Give the position of every malaria parasite, noting whether each is a trophozoite, schizont, or gametocyte.
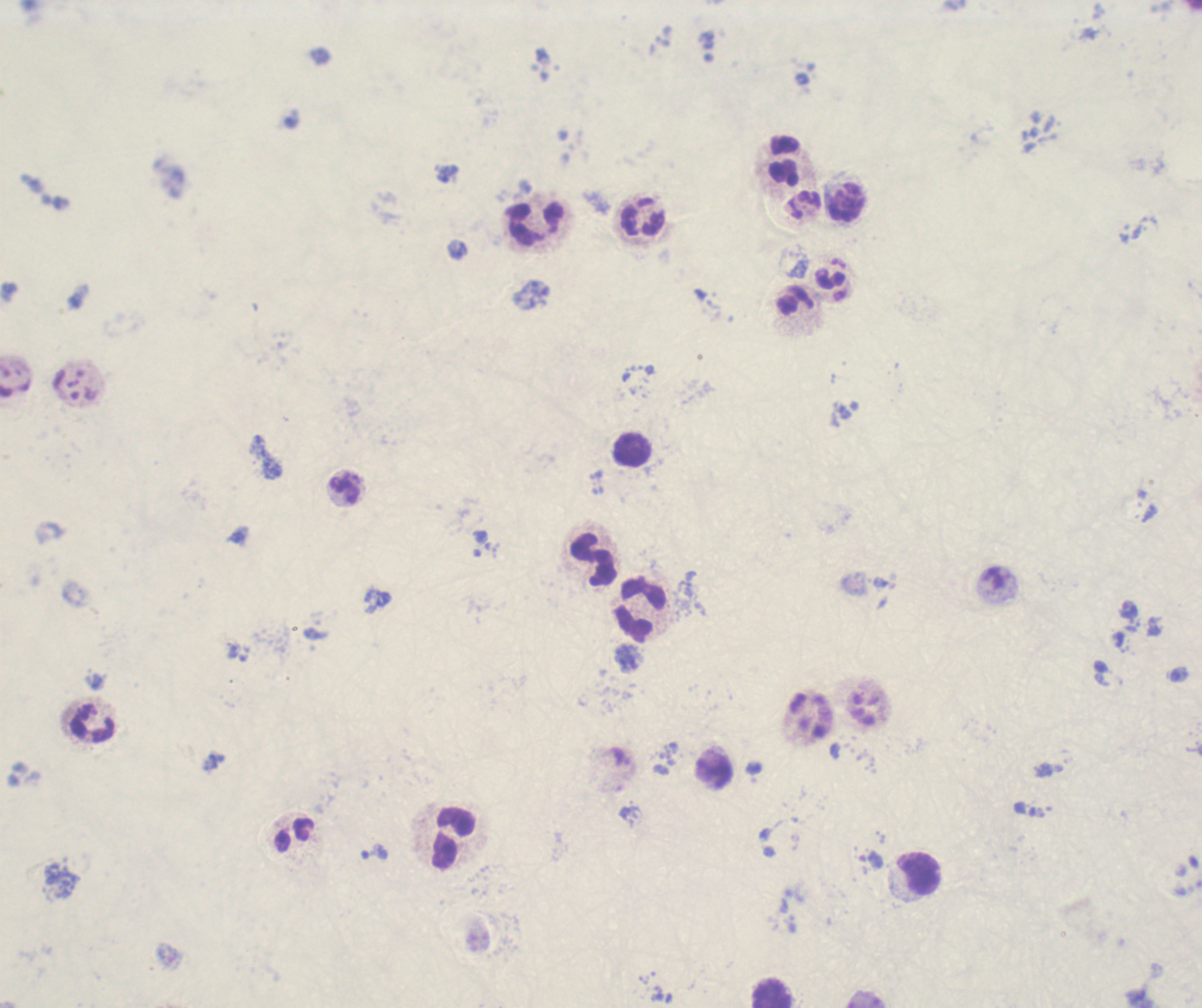
Approximate object centers, in pixels from the top-left corner.
Trophozoites: (x=374, y=852), (x=871, y=860).
No schizont or gametocyte forms observed.

coordinate format = approximate object centers, in pixels from the top-left corner
leukocyte locations = (x=783, y=160), (x=845, y=203), (x=642, y=218), (x=535, y=225), (x=630, y=450), (x=593, y=560), (x=642, y=612), (x=92, y=725), (x=714, y=773), (x=454, y=839), (x=919, y=875), (x=771, y=994)
context = previously used in an actual diagnosis
magnification = 100x
stain = Romanowsky
background quality = poor
field of view = single
preparation = thick blood smear
image size = 1202×1008 pixels